State the blood parasite species.
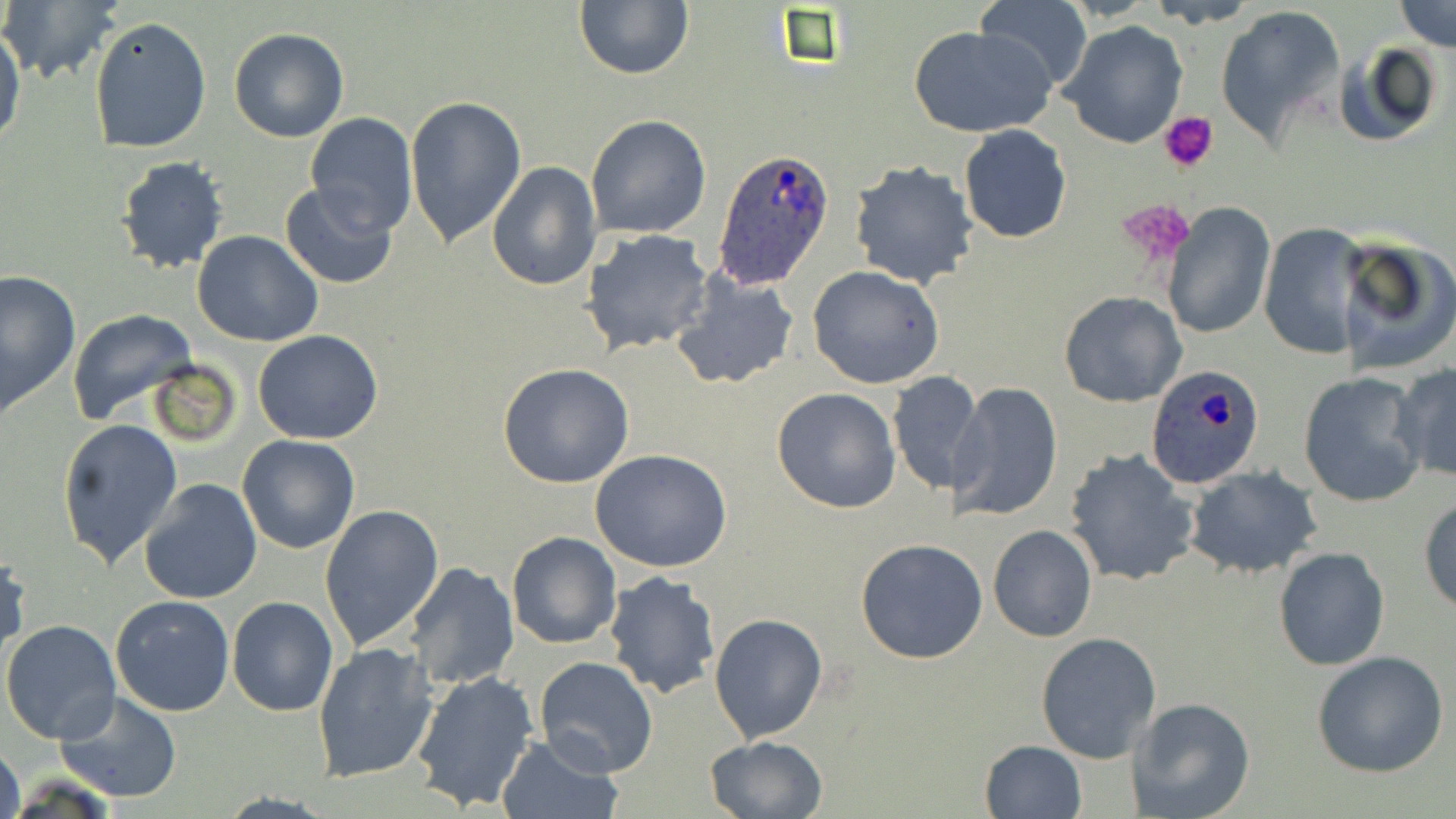

Plasmodium ovale.

field of view = single
Plasmodium ovale-infected red blood cell locations = approximate bounding boxes as (x1, y1, x2, y2) in pixels: (713, 147, 837, 289), (1145, 364, 1266, 489)
platelet locations = approximate bounding boxes as (x1, y1, x2, y2) in pixels: (1159, 113, 1218, 172), (1117, 199, 1196, 267)
stain = May-Grünwald-Giemsa
modality = light microscopy
preparation = thin blood film
magnification = 1000x
uninfected red blood cell locations = approximate bounding boxes as (x1, y1, x2, y2) in pixels: (1147, 0, 1259, 28), (1394, 0, 1455, 51), (1, 1, 124, 86), (574, 1, 693, 80), (974, 2, 1093, 93), (764, 5, 861, 76), (1213, 5, 1347, 148), (90, 15, 212, 154), (1058, 20, 1189, 149), (0, 21, 25, 151), (909, 23, 1054, 138), (228, 26, 350, 144), (1332, 41, 1443, 150), (405, 96, 527, 247), (302, 112, 418, 234), (586, 115, 711, 238), (958, 124, 1072, 243), (115, 156, 230, 274), (848, 158, 980, 288), (485, 159, 601, 291), (278, 181, 400, 290), (1162, 202, 1276, 339), (1258, 222, 1372, 360), (581, 229, 712, 355), (194, 230, 324, 347), (1334, 232, 1456, 375), (807, 265, 947, 389), (0, 270, 81, 412), (671, 270, 800, 390), (1058, 290, 1187, 407), (67, 308, 197, 426), (253, 329, 384, 444), (147, 360, 240, 448), (498, 362, 635, 488), (1392, 362, 1456, 484), (887, 370, 980, 497), (1296, 372, 1429, 508), (953, 382, 1063, 521), (771, 386, 903, 514), (57, 417, 181, 568), (237, 435, 360, 554), (1063, 448, 1199, 586), (591, 450, 733, 573), (1184, 465, 1322, 580), (139, 478, 263, 605), (1419, 496, 1456, 614), (320, 503, 444, 650), (987, 525, 1098, 642), (506, 532, 620, 649), (855, 538, 987, 664), (1273, 547, 1390, 671), (0, 552, 30, 659), (405, 562, 519, 690), (602, 571, 721, 699), (110, 595, 235, 716), (227, 596, 338, 716), (710, 610, 828, 743), (3, 612, 235, 730), (1, 619, 121, 746), (1036, 631, 1162, 762), (312, 641, 439, 782), (1312, 650, 1449, 777), (534, 656, 658, 778), (409, 671, 540, 813), (56, 691, 182, 802), (1131, 699, 1257, 819), (495, 735, 622, 819), (703, 736, 829, 819), (979, 739, 1087, 819), (0, 740, 24, 819)
image size = 1456×819 pixels